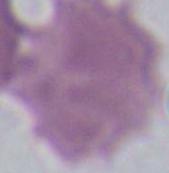

magnification: 1000x
modality: micrograph
identification: erythrocyte